Assess for Plasmodium parasites.
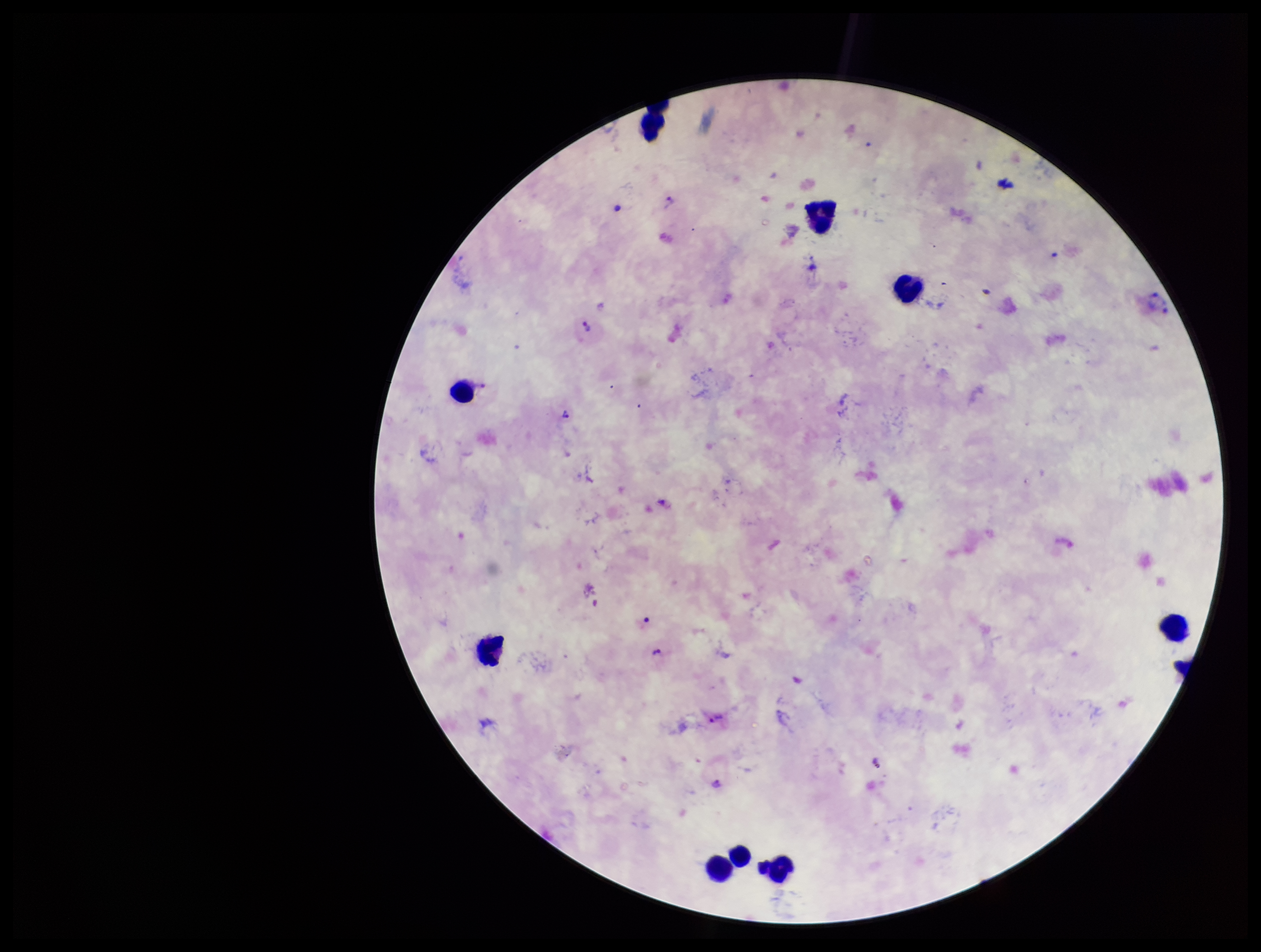
Identified.

Summary:
  - Image size: 1261×952 pixels
  - Stain: Giemsa
  - Capture: smartphone photograph through the microscope eyepiece
  - Species reported for this patient: Plasmodium vivax
  - Field of view: one from this slide
  - Preparation: thick blood smear
  - Leukocyte count: 9
  - Parasite count: 8
  - Patient malaria status: infected